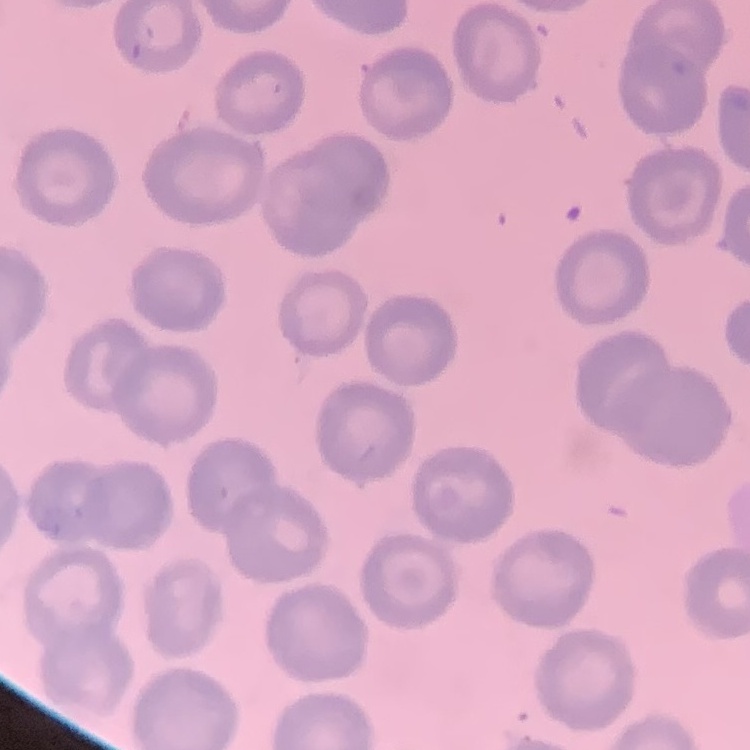

The erythrocytes exhibit no rouleaux formation. One tile cut from a larger photomicrograph. Thin blood smear. Stained with either Field's or Giemsa.